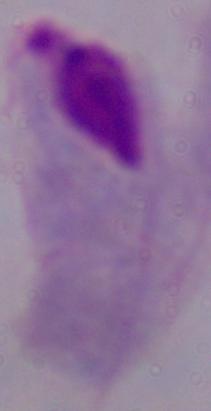
magnification = 1000x
modality = photomicrograph
identification = trichomonad